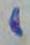

Summary:
  - Modality: micrograph
  - Magnification: 1000x
  - Identification: Toxoplasma gondii